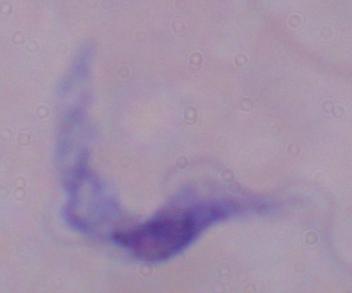 Photomicrograph. 1000x magnification. A trypanosome is seen.